Outline each Plasmodium ovale-infected red blood cell.
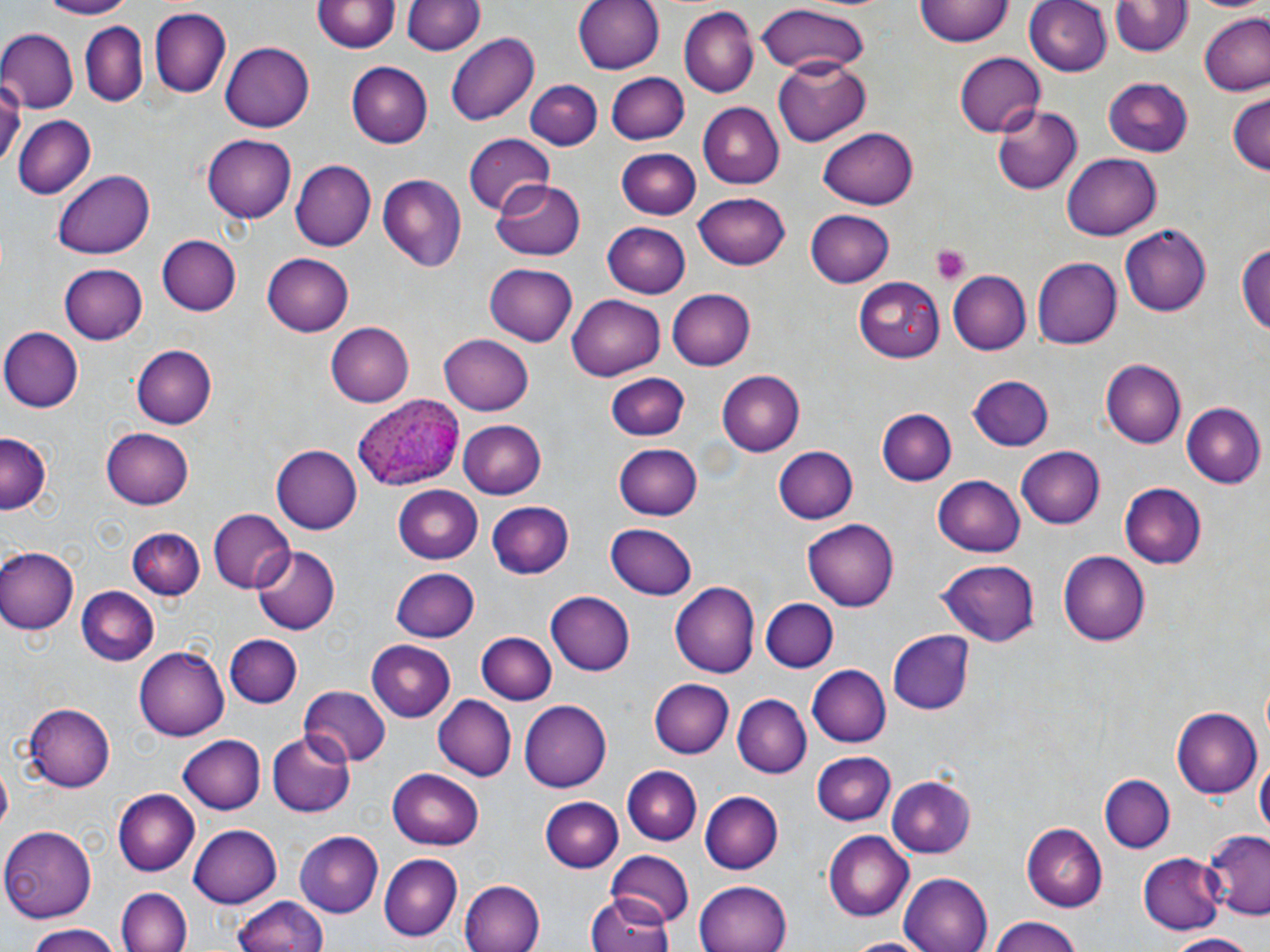
Approximate bounding boxes as [x1, y1, x2, y2] in pixels.
Plasmodium ovale-infected red blood cells: [355, 394, 460, 491].

slide-level diagnosis = Plasmodium ovale
image size = 1270×952 pixels
stain = May-Grünwald-Giemsa
field of view = one of a larger specimen
modality = light microscopy
platelet locations = approximate bounding boxes as [x1, y1, x2, y2] in pixels: [931, 245, 970, 285]
uninfected red blood cell locations = approximate bounding boxes as [x1, y1, x2, y2] in pixels: [32, 0, 142, 19], [573, 0, 663, 75], [915, 0, 1014, 48], [1026, 0, 1113, 77], [1188, 0, 1270, 14], [313, 1, 397, 55], [401, 1, 484, 57], [1112, 1, 1191, 58], [756, 4, 871, 79], [150, 8, 230, 98], [680, 8, 757, 97], [1199, 15, 1270, 97], [80, 21, 150, 106], [0, 29, 78, 111], [446, 33, 540, 127], [220, 40, 315, 133], [954, 53, 1046, 137], [773, 55, 871, 145], [345, 61, 432, 148], [604, 73, 688, 146], [1105, 76, 1193, 155], [0, 78, 24, 166], [526, 81, 602, 150], [1227, 94, 1270, 178], [994, 103, 1082, 194], [695, 104, 782, 189], [11, 113, 96, 198], [818, 128, 916, 208], [463, 133, 554, 213], [201, 135, 296, 223], [618, 146, 699, 219], [1062, 152, 1160, 241], [291, 161, 374, 250], [52, 170, 155, 261], [376, 174, 466, 272], [491, 178, 583, 261], [693, 192, 790, 269], [805, 209, 895, 287], [601, 222, 690, 298], [1120, 222, 1212, 315], [157, 234, 240, 316], [1237, 234, 1270, 345], [262, 253, 354, 336], [1033, 258, 1122, 349], [59, 261, 148, 344], [484, 263, 578, 347], [948, 270, 1032, 355], [855, 275, 945, 363], [666, 289, 754, 370], [567, 292, 666, 381], [326, 322, 414, 408], [1, 327, 81, 412], [439, 333, 534, 416], [132, 345, 215, 428], [1103, 360, 1187, 448], [714, 368, 803, 457], [609, 371, 688, 441], [963, 375, 1054, 453], [1182, 403, 1265, 488], [878, 408, 955, 485], [457, 417, 546, 497], [103, 426, 194, 510], [0, 435, 50, 516], [615, 443, 703, 520], [272, 444, 362, 532], [773, 446, 859, 523], [1014, 447, 1104, 529], [932, 475, 1026, 555], [392, 484, 485, 562], [1121, 484, 1206, 570], [486, 501, 574, 579], [208, 510, 293, 595], [801, 518, 898, 611], [607, 522, 698, 600], [129, 525, 204, 598], [0, 545, 78, 635], [252, 545, 339, 635], [1058, 551, 1149, 645], [935, 558, 1041, 649], [391, 568, 480, 642], [673, 582, 761, 677], [76, 587, 160, 668], [546, 592, 636, 676], [761, 599, 838, 671], [476, 632, 556, 706], [888, 632, 974, 715], [224, 634, 302, 707], [366, 639, 455, 720], [136, 645, 229, 741], [806, 664, 891, 748], [650, 678, 733, 758], [298, 686, 391, 768], [432, 695, 514, 782], [733, 695, 810, 777], [518, 697, 611, 789], [25, 703, 115, 791], [1171, 707, 1260, 799], [265, 731, 356, 817], [179, 735, 268, 814], [812, 750, 896, 827], [1256, 755, 1268, 844], [388, 766, 485, 847], [622, 766, 701, 843], [1101, 773, 1174, 852], [888, 775, 975, 856], [111, 788, 199, 877], [700, 791, 782, 873], [539, 796, 622, 872], [1023, 823, 1107, 910], [188, 825, 280, 907], [0, 826, 99, 921], [295, 830, 384, 917], [823, 830, 914, 921], [1204, 831, 1270, 919], [606, 851, 694, 927], [1141, 852, 1221, 935], [378, 853, 462, 941], [899, 872, 994, 952], [460, 880, 546, 952], [694, 881, 793, 952], [119, 888, 192, 952], [231, 894, 328, 951], [589, 895, 675, 952], [987, 918, 1087, 952], [25, 927, 121, 952], [1162, 932, 1266, 950], [841, 936, 932, 952]
magnification = 1000x
preparation = thin blood film